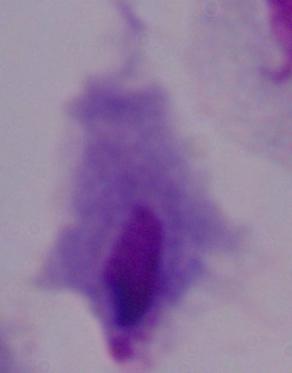

Summary:
  - Magnification: 1000x
  - Modality: photomicrograph
  - Identification: trichomonad